Draw a bounding box around every malaria parasite, every leukocyte, and every artifact (stain precipitate or debris).
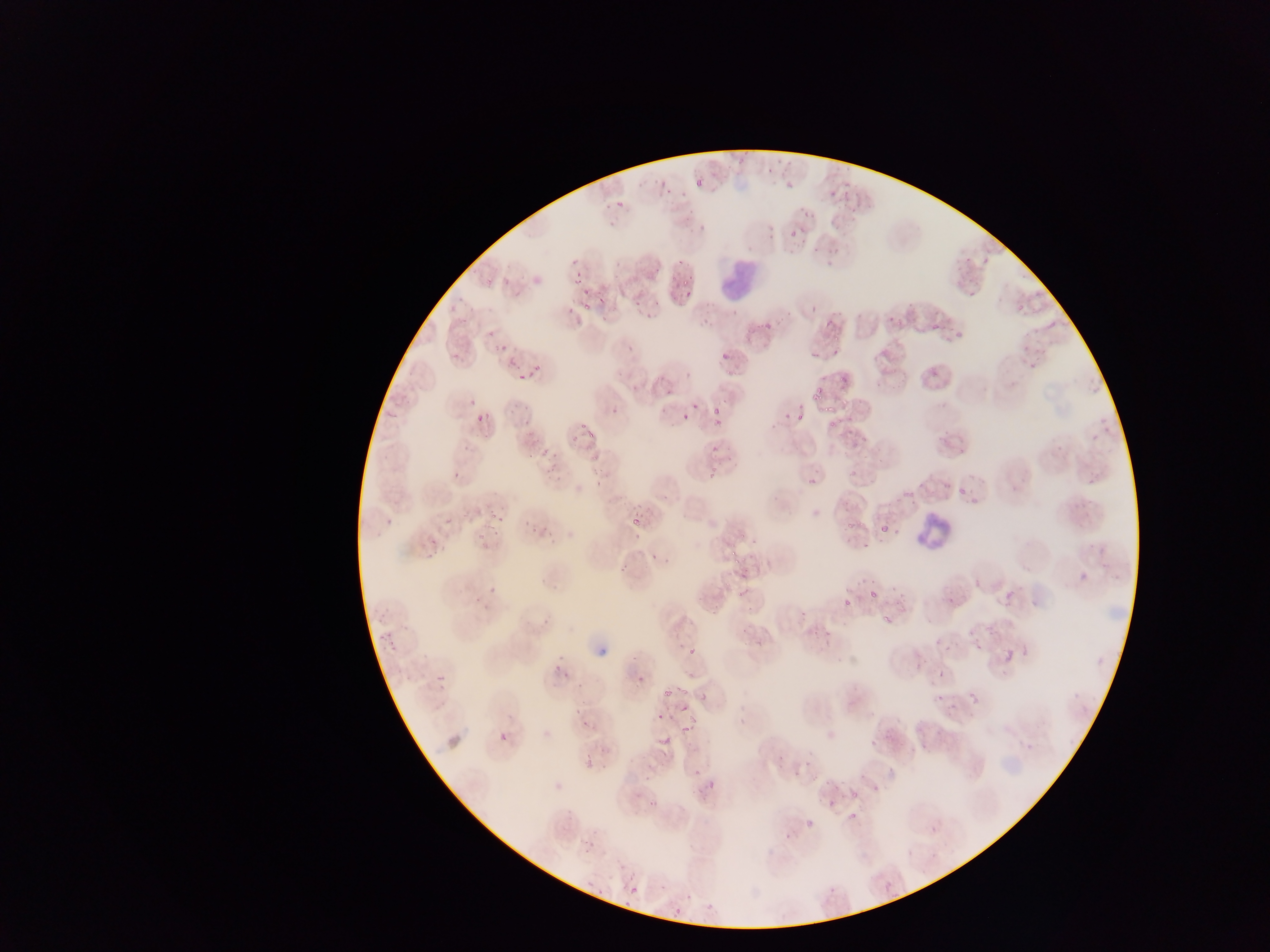
Approximate bounding boxes as {left, top, right, bottom} in pixels.
Malaria parasites: {776, 173, 805, 191}, {693, 176, 704, 188}, {784, 219, 799, 237}, {963, 250, 970, 264}, {566, 272, 582, 286}, {676, 277, 690, 286}, {967, 285, 978, 299}, {683, 289, 692, 296}, {573, 297, 595, 316}, {882, 307, 901, 330}, {928, 312, 946, 333}, {1045, 318, 1060, 333}, {945, 324, 970, 345}, {828, 329, 842, 344}, {719, 342, 740, 360}, {802, 345, 817, 358}, {450, 351, 463, 364}, {839, 368, 849, 392}, {512, 369, 534, 384}, {814, 384, 827, 399}, {707, 400, 727, 419}, {822, 403, 836, 414}, {842, 403, 854, 412}, {680, 406, 690, 425}, {472, 407, 494, 431}, {793, 408, 808, 423}, {779, 409, 792, 422}, {711, 415, 729, 430}, {826, 419, 841, 430}, {583, 423, 601, 443}, {862, 434, 874, 447}, {848, 435, 859, 448}, {536, 437, 559, 462}, {708, 443, 723, 453}, {590, 453, 603, 461}, {544, 464, 557, 479}, {848, 466, 858, 479}, {588, 468, 610, 489}, {806, 476, 819, 489}, {957, 477, 974, 499}, {902, 489, 915, 504}, {489, 504, 506, 523}, {631, 510, 650, 529}, {528, 516, 551, 535}, {846, 519, 857, 533}, {878, 520, 891, 535}, {893, 526, 902, 541}, {477, 527, 496, 546}, {862, 542, 871, 549}, {726, 545, 738, 556}, {729, 552, 746, 579}, {998, 582, 1017, 608}, {738, 588, 751, 602}, {872, 589, 881, 597}, {943, 591, 961, 609}, {843, 597, 854, 608}, {879, 606, 897, 623}, {974, 643, 984, 653}, {687, 645, 698, 659}, {999, 647, 1018, 667}, {937, 668, 948, 681}, {435, 674, 449, 690}, {676, 682, 689, 696}, {662, 689, 673, 702}, {937, 689, 949, 700}, {688, 690, 707, 706}, {968, 691, 982, 706}, {676, 701, 694, 727}, {650, 710, 665, 724}, {670, 723, 699, 733}, {654, 730, 673, 751}, {498, 731, 510, 745}, {582, 738, 604, 768}, {688, 769, 699, 778}, {701, 770, 721, 790}, {849, 786, 857, 800}, {645, 795, 662, 808}, {843, 809, 857, 822}, {801, 812, 822, 828}, {880, 877, 898, 897}, {628, 884, 641, 897}.
Leukocytes: {724, 260, 760, 303}, {914, 513, 958, 552}.

{
  "country": "Ghana",
  "image_size": "1270×952 pixels",
  "field_of_view": "single",
  "capture": "mobile-phone photograph through a microscope",
  "preparation": "thin blood smear"
}